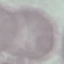

malaria status = uninfected
image type = automatically extracted cell patch, resized to 64 × 64 pixels
stain = Giemsa
preparation = thin blood film
capture = smartphone camera at the microscope eyepiece